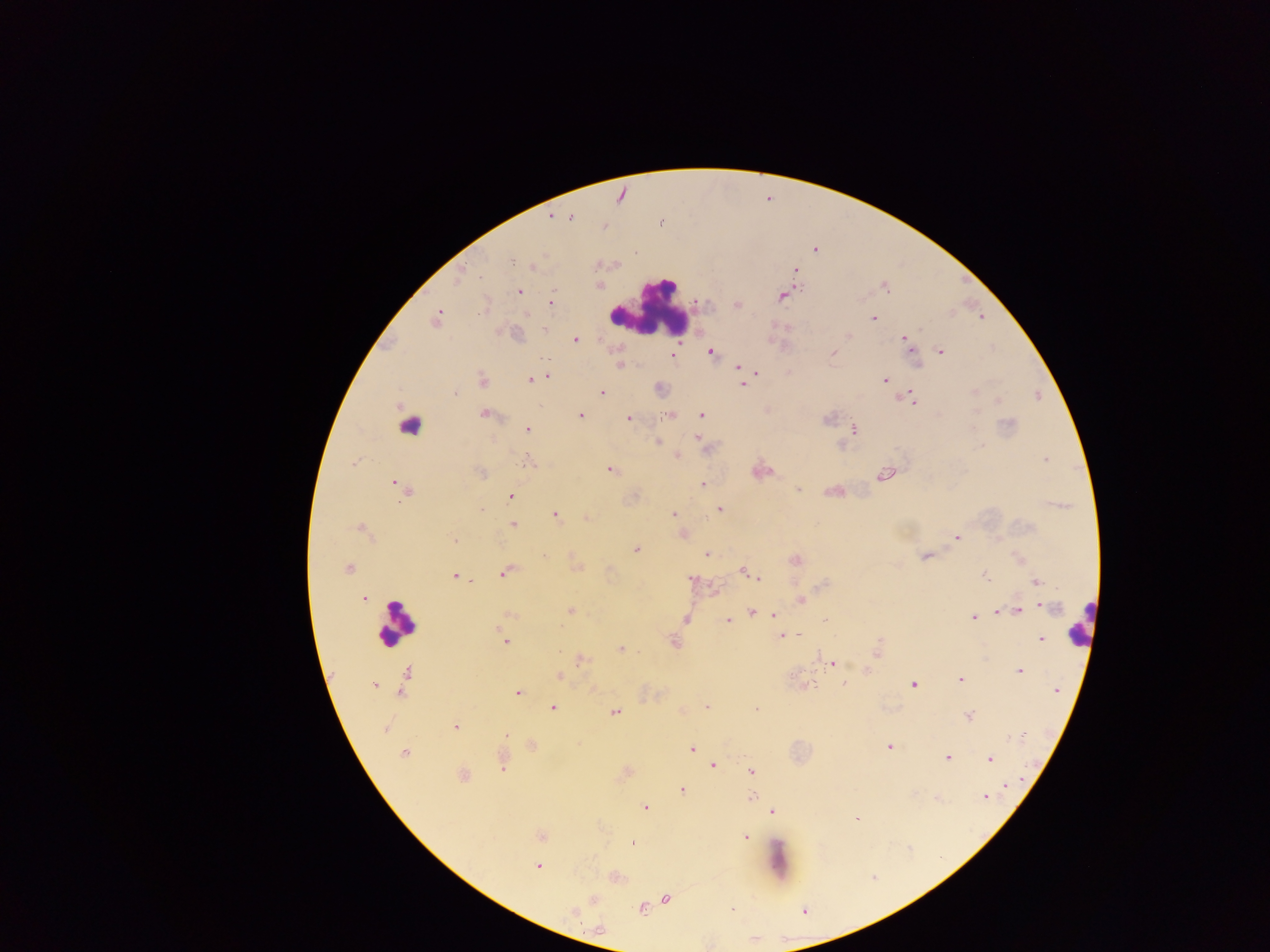

Approximate centers as {x, y} in pixels.
Summary:
  - Leukocyte locations: {652, 308}, {411, 424}, {395, 625}, {1081, 633}, {782, 864}
  - Plasmodium parasite locations: {549, 217}, {570, 217}, {511, 259}, {519, 291}, {782, 298}, {551, 303}, {440, 310}, {527, 314}, {980, 316}, {872, 320}, {576, 339}, {902, 339}, {710, 352}, {833, 352}, {940, 352}, {619, 362}, {737, 367}, {758, 371}, {547, 375}, {529, 378}, {883, 378}, {742, 386}, {602, 391}, {916, 402}, {582, 415}, {670, 415}, {702, 415}, {628, 418}, {852, 429}, {527, 430}, {698, 437}, {658, 440}, {677, 455}, {1044, 458}, {353, 462}, {528, 463}, {609, 470}, {882, 475}, {393, 483}, {702, 484}, {798, 489}, {512, 496}, {481, 509}, {720, 509}, {673, 513}, {554, 515}, {513, 523}, {357, 528}, {682, 533}, {955, 536}, {452, 540}, {637, 548}, {706, 552}, {545, 554}, {577, 567}, {349, 568}, {741, 569}, {504, 573}, {454, 575}, {757, 577}, {1036, 581}, {364, 597}, {361, 598}, {800, 599}, {1042, 606}, {1020, 610}, {571, 611}, {751, 612}, {997, 612}, {773, 615}, {972, 615}, {686, 618}, {825, 620}, {727, 622}, {781, 636}, {1041, 639}, {504, 641}, {623, 647}, {578, 663}, {831, 663}, {1021, 673}, {405, 675}, {960, 678}, {844, 684}, {914, 685}, {379, 687}, {1056, 691}, {516, 692}, {707, 705}, {551, 707}, {755, 707}, {614, 710}, {681, 710}, {968, 716}, {386, 725}, {455, 725}, {506, 734}, {890, 748}, {692, 751}, {405, 753}, {946, 756}, {989, 758}, {503, 765}, {713, 766}, {752, 772}, {1007, 783}, {681, 790}, {752, 796}, {985, 799}, {644, 804}, {773, 810}, {856, 820}, {744, 835}, {632, 843}, {535, 866}, {595, 899}, {666, 899}, {642, 909}
  - Image size: 1270×952 pixels
  - Country: Ghana
  - Field of view: single
  - Capture: mobile-phone photograph through a microscope
  - Preparation: thick blood smear